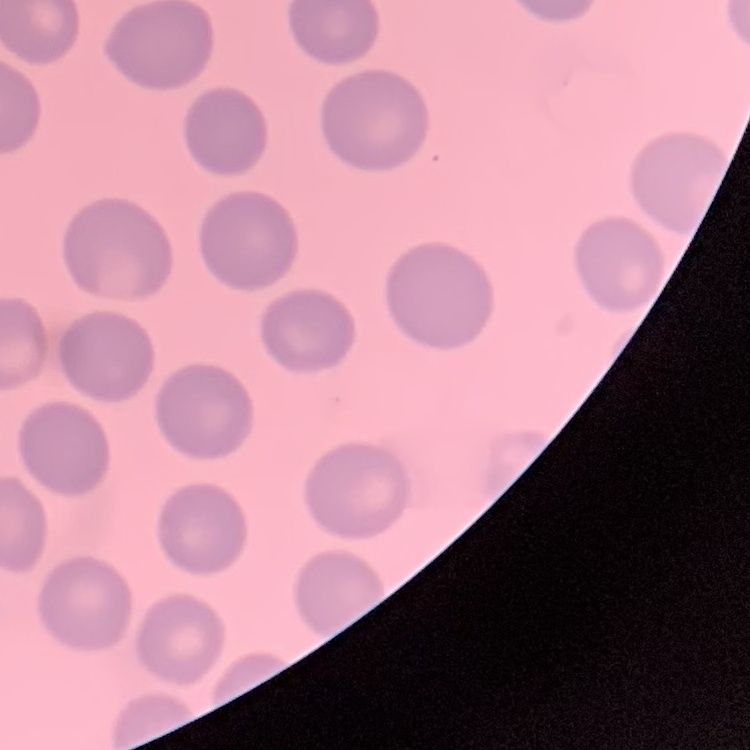

erythrocyte morphology = no rouleaux formation
preparation = thin blood smear
stain = Field's or Giemsa
image type = square crop of a larger photomicrograph